Identify the malaria species.
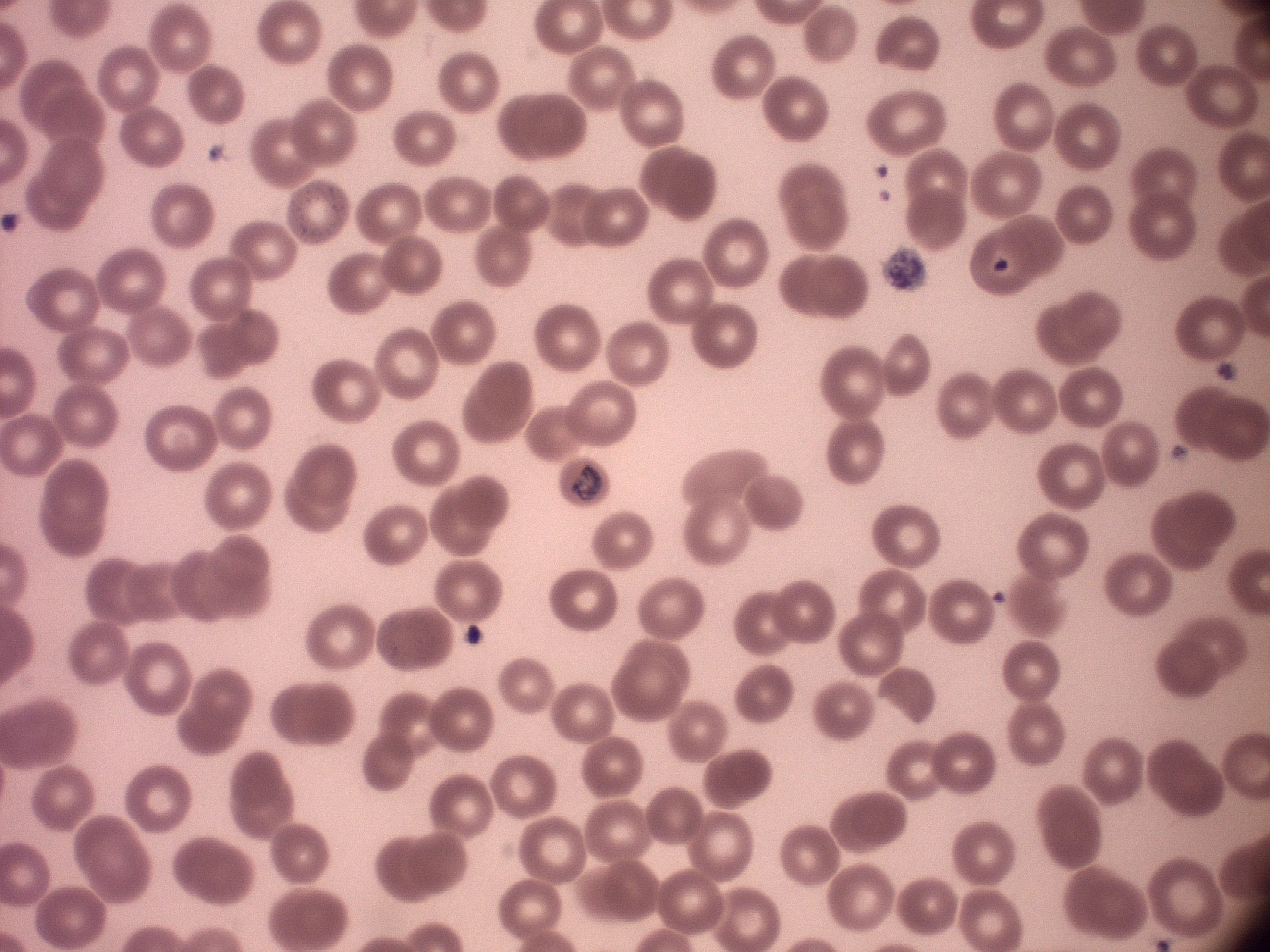

Plasmodium malariae.

field of view = one from this slide
trophozoite locations = approximate bounding boxes as named x1/y1/x2/y2 corners in pixels, from the source annotation, which is not necessarily exhaustive: (x1=573, y1=465, x2=602, y2=502)
stain = Giemsa
microscope = Leica DM2000 with built-in camera
image size = 1270×952 pixels
preparation = thin blood smear
magnification = 100x